Name the cell type shown.
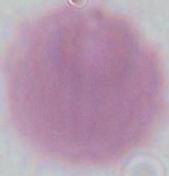
An erythrocyte.

magnification = 1000x
modality = micrograph